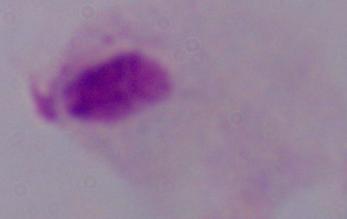
A trichomonad is shown. 1000x magnification. Photomicrograph.